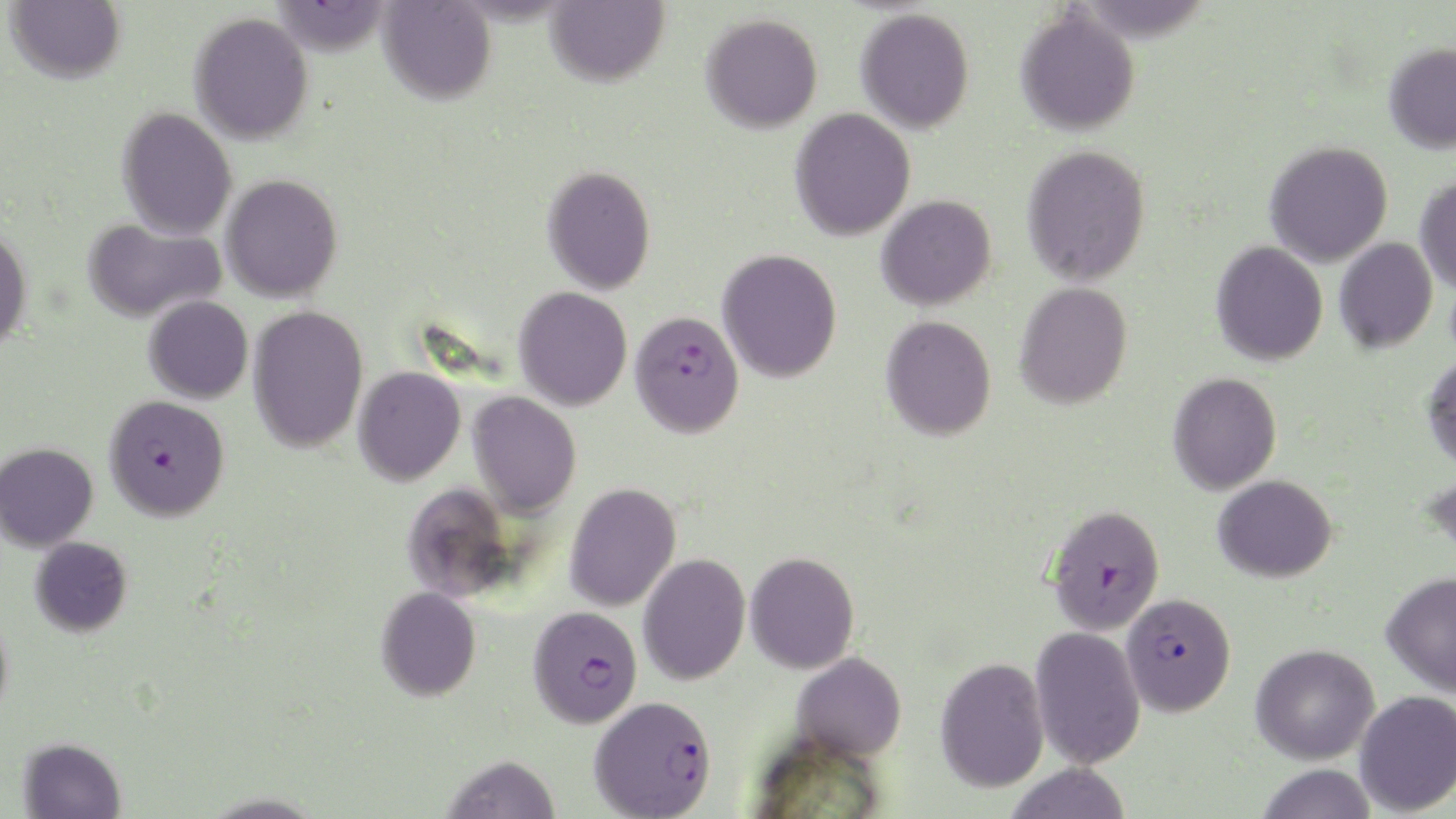

Summary:
  - Coordinate format: approximate bounding boxes as (x1, y1, x2, y2) in pixels
  - Plasmodium falciparum-infected red blood cell locations: (629, 310, 744, 438), (104, 394, 229, 521), (1045, 504, 1165, 635), (1121, 592, 1236, 716), (527, 605, 644, 728), (588, 696, 717, 819)
  - Uninfected red blood cell locations: (6, 0, 126, 84), (269, 0, 394, 57), (378, 0, 496, 105), (545, 0, 669, 87), (856, 8, 975, 134), (1015, 8, 1140, 136), (189, 12, 314, 145), (700, 13, 823, 133), (1383, 42, 1456, 154), (117, 107, 237, 240), (789, 108, 915, 241), (1264, 141, 1393, 267), (1021, 144, 1151, 286), (542, 165, 656, 295), (221, 174, 343, 303), (1415, 175, 1456, 293), (876, 195, 996, 310), (81, 218, 225, 324), (0, 225, 33, 352), (1334, 237, 1437, 353), (1210, 241, 1328, 366), (717, 248, 842, 383), (1014, 282, 1133, 409), (513, 286, 632, 411), (143, 295, 253, 404), (248, 305, 368, 453), (880, 315, 997, 441), (1422, 351, 1456, 474), (353, 366, 465, 486), (1168, 372, 1282, 495), (468, 391, 581, 519), (0, 442, 98, 551), (1422, 469, 1456, 575), (1213, 475, 1337, 582), (401, 482, 518, 603), (565, 482, 681, 612), (30, 536, 132, 636), (745, 551, 859, 674), (638, 553, 750, 685), (1381, 570, 1456, 697), (375, 586, 481, 701), (0, 608, 13, 726), (1030, 625, 1145, 769), (1251, 643, 1380, 765), (791, 652, 907, 761), (935, 656, 1049, 793), (1354, 690, 1456, 816), (18, 737, 126, 818), (441, 754, 562, 819), (1003, 763, 1132, 819), (1255, 763, 1378, 819), (200, 791, 326, 819)
  - Slide-level diagnosis: Plasmodium falciparum
  - Field of view: one of a larger specimen
  - Preparation: thin blood film
  - Magnification: 1000x
  - Modality: optical microscopy
  - Stain: May-Grünwald-Giemsa
  - Image size: 1456×819 pixels